State the blood parasite species.
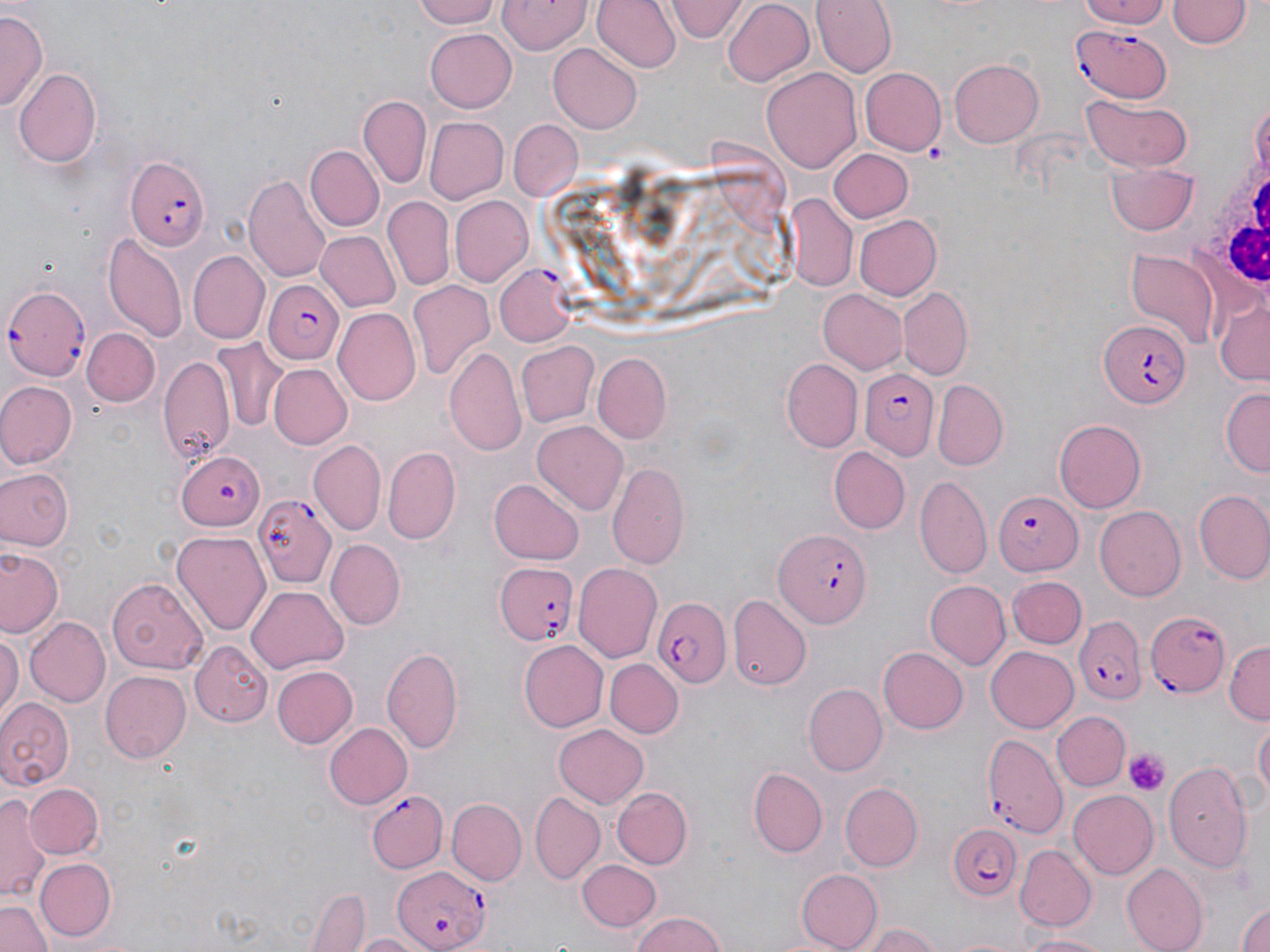

Plasmodium falciparum.

Summary:
  - Coordinate format: approximate bounding boxes as [x1, y1, x2, y2] in pixels
  - White blood cell locations: [1204, 152, 1270, 299]
  - Platelet locations: [1125, 749, 1170, 793]
  - Plasmodium falciparum-infected red blood cell locations: [1073, 20, 1172, 104], [122, 153, 212, 250], [495, 265, 577, 346], [265, 279, 343, 362], [2, 280, 93, 378], [1099, 320, 1194, 408], [859, 369, 942, 458], [175, 451, 263, 531], [993, 492, 1083, 575], [254, 493, 336, 589], [773, 529, 872, 626], [491, 560, 579, 649], [652, 596, 732, 688], [1144, 609, 1231, 699], [1075, 618, 1146, 706], [981, 731, 1066, 841], [365, 791, 447, 873], [944, 822, 1022, 903], [392, 863, 488, 951]
  - Uninfected red blood cell locations: [410, 0, 502, 28], [593, 0, 680, 75], [667, 0, 746, 42], [721, 0, 817, 88], [812, 0, 894, 77], [1075, 0, 1175, 28], [496, 1, 591, 56], [1168, 2, 1249, 50], [0, 11, 45, 113], [423, 28, 518, 111], [549, 43, 643, 132], [948, 57, 1045, 147], [11, 65, 103, 170], [763, 66, 861, 172], [860, 68, 944, 154], [358, 96, 431, 187], [1081, 96, 1191, 170], [1250, 96, 1269, 184], [425, 115, 508, 203], [509, 120, 582, 200], [304, 146, 383, 232], [829, 148, 912, 222], [1108, 162, 1200, 236], [245, 171, 334, 281], [451, 196, 532, 285], [784, 196, 856, 292], [383, 199, 453, 291], [852, 214, 939, 299], [315, 230, 400, 312], [103, 235, 186, 343], [1127, 246, 1218, 345], [187, 250, 270, 344], [407, 282, 495, 380], [818, 288, 909, 375], [897, 288, 971, 378], [1212, 295, 1269, 389], [333, 308, 421, 405], [83, 328, 160, 406], [212, 339, 286, 431], [518, 342, 598, 427], [444, 347, 526, 458], [592, 354, 671, 441], [158, 356, 236, 464], [781, 360, 861, 453], [267, 364, 352, 450], [934, 379, 1008, 469], [0, 380, 77, 469], [1220, 388, 1270, 474], [1057, 419, 1146, 511], [533, 422, 628, 516], [310, 439, 386, 533], [827, 447, 910, 533], [382, 449, 459, 545], [608, 463, 689, 570], [0, 465, 75, 551], [917, 476, 990, 577], [489, 478, 583, 563], [1194, 490, 1270, 584], [1095, 506, 1186, 601], [171, 530, 274, 636], [327, 539, 404, 628], [3, 547, 62, 639], [574, 563, 663, 663], [1006, 575, 1085, 649], [107, 576, 210, 670], [926, 579, 1010, 670], [246, 585, 348, 674], [729, 595, 811, 692], [25, 616, 111, 708], [0, 628, 21, 723], [517, 640, 608, 732], [1226, 641, 1270, 722], [191, 643, 271, 723], [986, 644, 1081, 732], [881, 645, 969, 734], [382, 647, 463, 754], [606, 657, 684, 737], [269, 665, 358, 749], [100, 670, 192, 762], [804, 684, 887, 775], [0, 696, 75, 787], [1054, 711, 1128, 791], [1254, 718, 1269, 806], [324, 723, 413, 808], [553, 724, 649, 807], [1164, 759, 1256, 869], [747, 765, 828, 858], [838, 780, 922, 870], [23, 783, 103, 859], [613, 788, 693, 868], [1069, 790, 1159, 879], [0, 791, 49, 902], [531, 792, 605, 883], [446, 799, 525, 884], [1014, 846, 1095, 931], [34, 856, 116, 942], [577, 860, 660, 930], [1122, 864, 1208, 952], [793, 868, 882, 952], [306, 889, 371, 951], [1234, 897, 1270, 952], [0, 898, 51, 952], [627, 911, 730, 952], [865, 924, 941, 951], [351, 931, 432, 952], [1021, 932, 1112, 951]
  - Stain: May-Grünwald-Giemsa
  - Magnification: 1000x
  - Preparation: thin blood film
  - Modality: optical microscopy
  - Field of view: single
  - Image size: 1270×952 pixels